Describe the morphology of the erythrocytes.
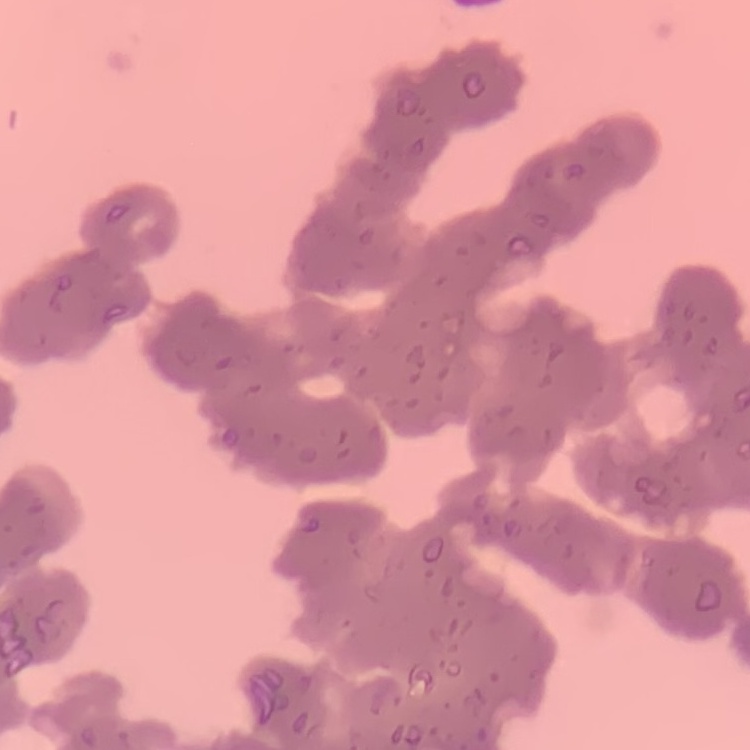
Rouleaux formation.

image_type: one tile cut from a larger photomicrograph
stain: Field's or Giemsa
preparation: thin peripheral smear